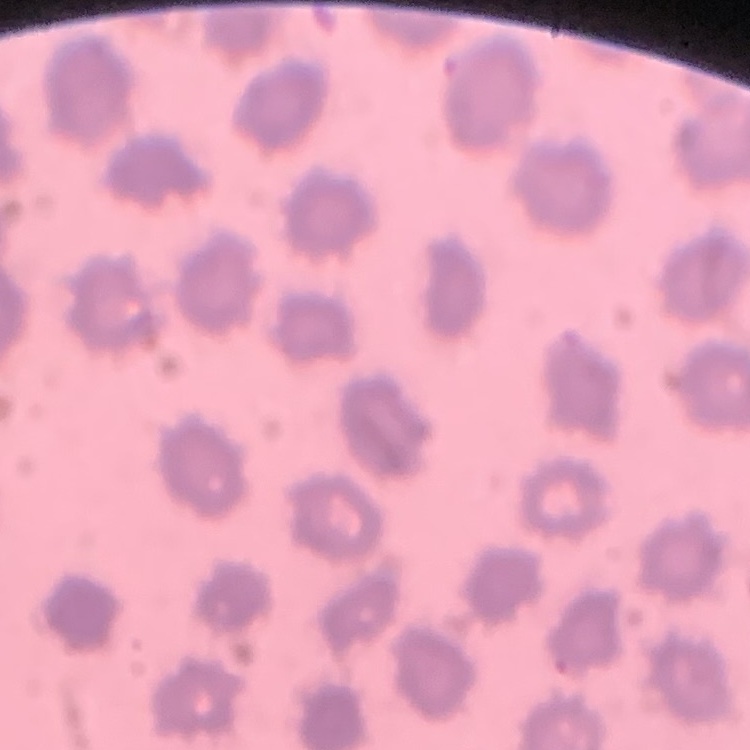
erythrocyte morphology = no rouleaux formation
image type = square crop of a larger photomicrograph
stain = Field's or Giemsa
preparation = thin peripheral smear